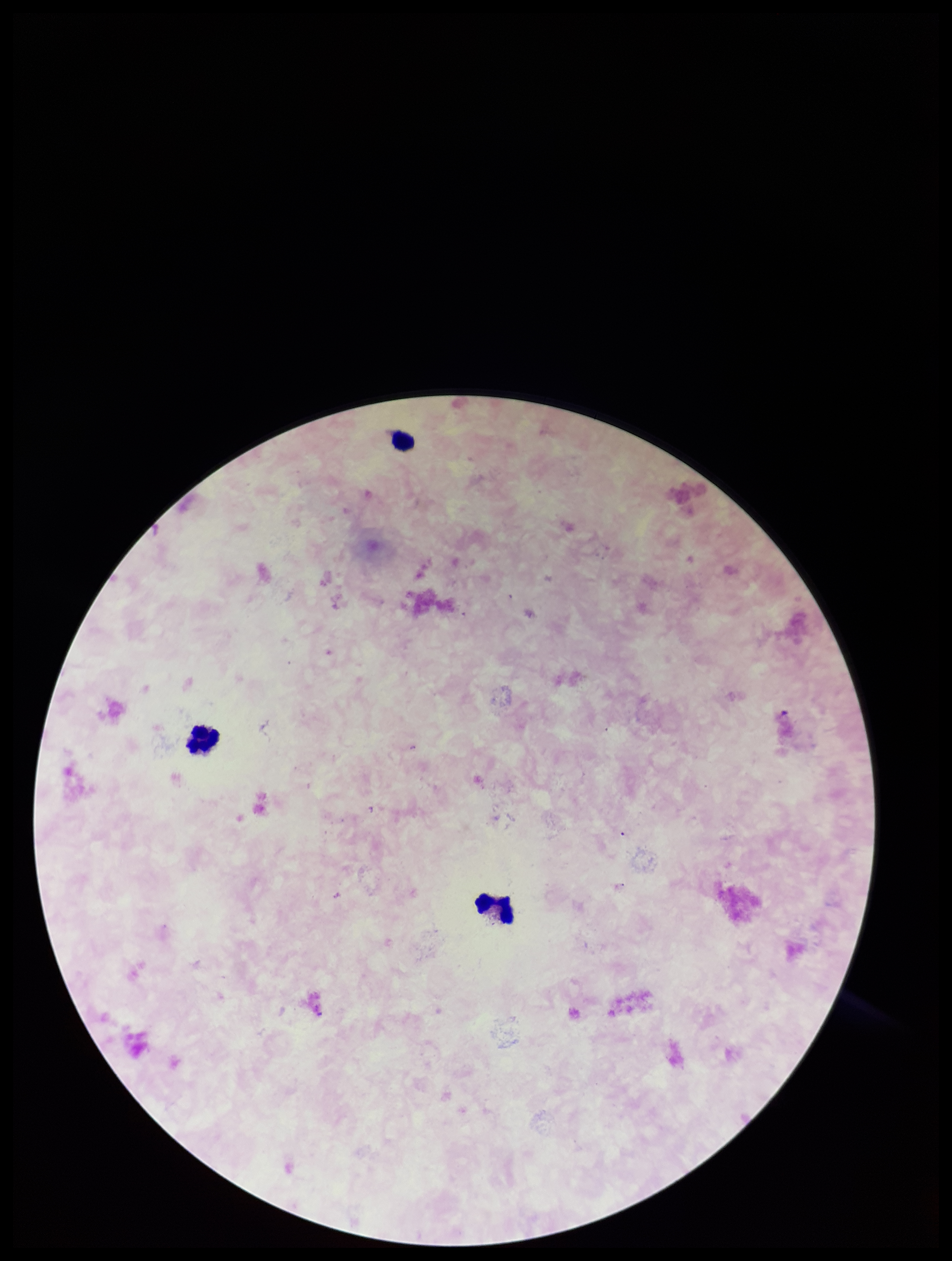
One field from this slide. Patient malaria status: negative. Preparation: thick. Plasmodium parasites: none identified. Stained with Giemsa. Image is 952×1261 pixels. Photographed through the microscope eyepiece with a smartphone camera. Parasite count: 0. Leukocyte count: 3.